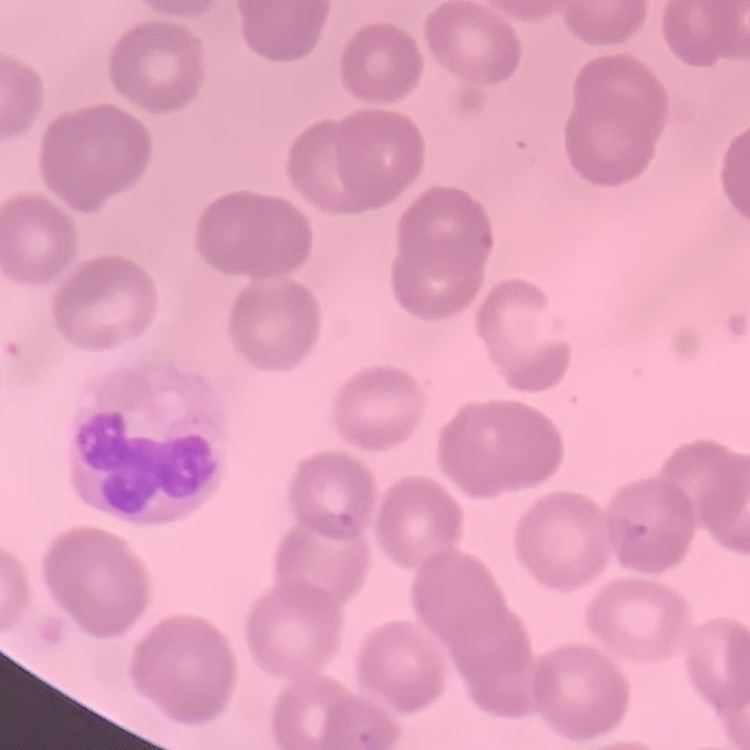

Summary:
  - Erythrocyte morphology: no rouleaux formation
  - Preparation: thin peripheral smear
  - Image type: square crop of a larger photomicrograph
  - Stain: Field's or Giemsa